Give the extent of all Plasmodium parasites.
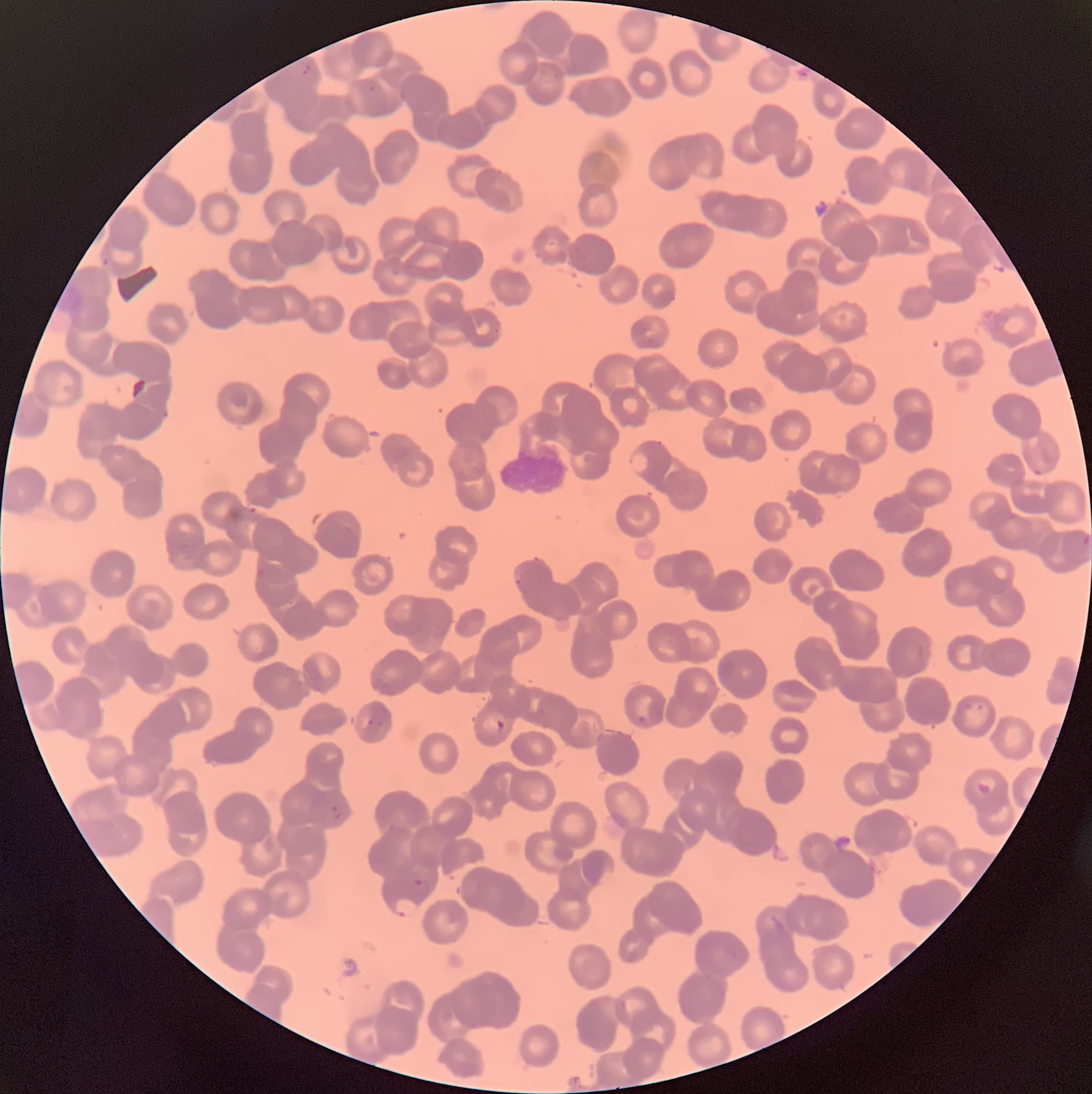

Approximate bounding boxes as named x1/y1/x2/y2 corners in pixels.
Plasmodium parasites: (x1=301, y1=63, x2=315, y2=81), (x1=367, y1=83, x2=377, y2=95), (x1=102, y1=255, x2=112, y2=270), (x1=627, y1=451, x2=651, y2=474), (x1=1032, y1=467, x2=1045, y2=477), (x1=1081, y1=533, x2=1092, y2=547), (x1=637, y1=714, x2=647, y2=724), (x1=366, y1=718, x2=375, y2=727), (x1=494, y1=719, x2=506, y2=733), (x1=976, y1=780, x2=993, y2=797), (x1=321, y1=804, x2=343, y2=824), (x1=414, y1=878, x2=434, y2=894), (x1=393, y1=895, x2=420, y2=918).

modality = light microscopy
red blood cell morphology = rouleaux formation
preparation = thin blood film
image size = 1092×1094 pixels